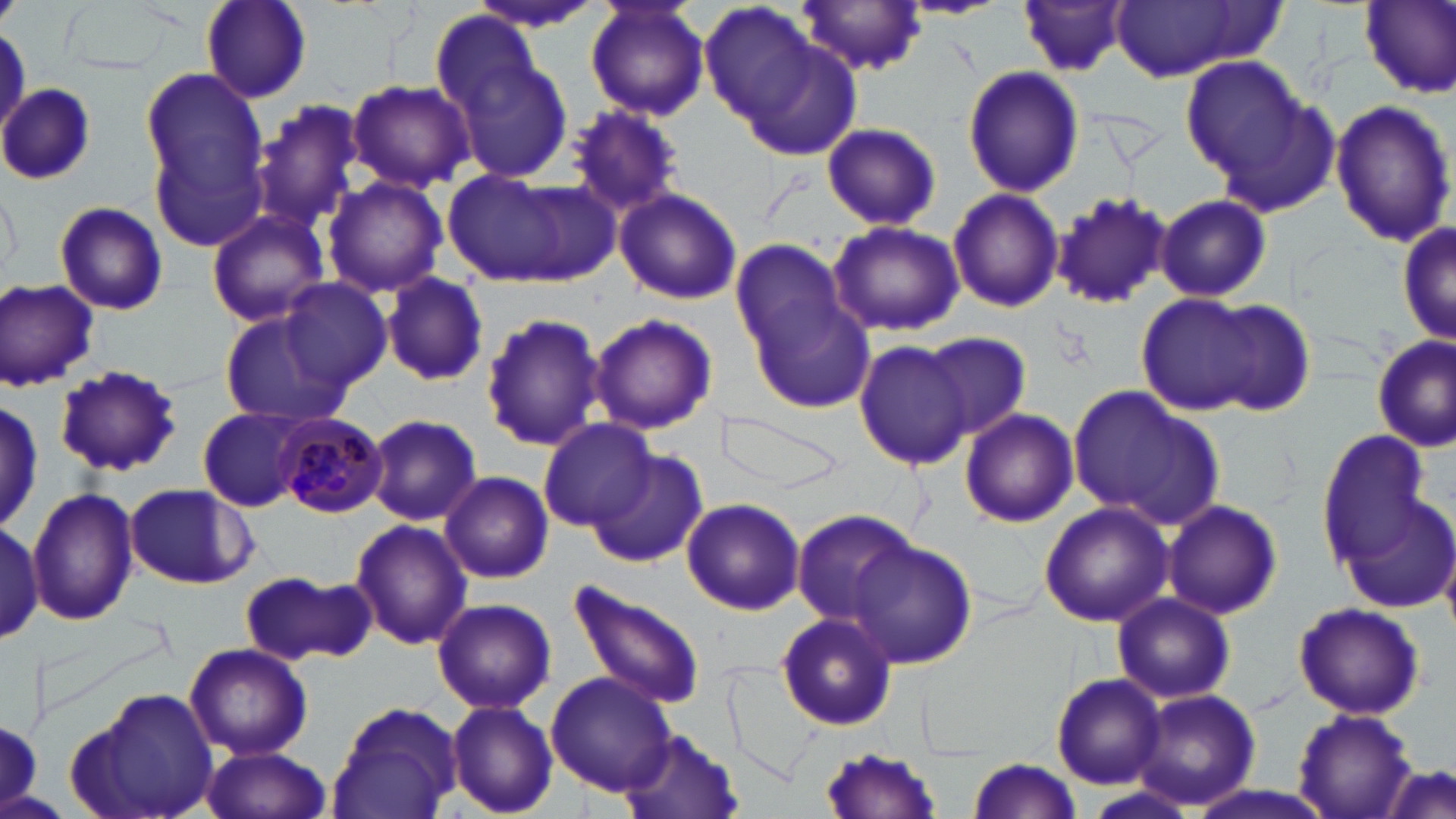
slide-level diagnosis = Plasmodium malariae
field of view = single
uninfected red blood cell locations = approximate bounding boxes as (x1,y1)-(x2,y2) corner pairs in pixels: (196,0)-(311,103), (464,0)-(609,34), (585,0)-(710,123), (901,0)-(1008,20), (1107,0)-(1276,82), (1358,0)-(1456,96), (696,1)-(826,129), (799,1)-(929,76), (1019,1)-(1130,78), (728,24)-(864,161), (437,32)-(573,188), (1180,54)-(1309,188), (961,64)-(1085,198), (139,67)-(267,201), (347,80)-(473,191), (0,82)-(96,184), (1330,97)-(1454,250), (257,101)-(365,228), (564,104)-(686,218), (820,122)-(941,231), (151,135)-(270,257), (443,170)-(597,287), (321,176)-(447,298), (0,185)-(23,284), (947,187)-(1065,314), (615,189)-(742,306), (1051,189)-(1172,310), (1154,194)-(1272,303), (53,201)-(169,316), (203,209)-(332,326), (1395,213)-(1454,352), (829,221)-(964,337), (731,239)-(848,355), (381,271)-(489,387), (277,277)-(392,391), (1,280)-(101,390), (748,289)-(874,412), (1136,292)-(1293,418), (1202,303)-(1318,415), (216,311)-(349,425), (480,311)-(605,451), (586,313)-(720,434), (920,331)-(1030,442), (1371,332)-(1455,452), (853,338)-(975,470), (53,365)-(183,477), (1069,387)-(1225,528), (714,406)-(848,499), (196,407)-(312,512), (960,408)-(1079,528), (365,413)-(482,526), (538,419)-(657,531), (1316,428)-(1435,568), (587,453)-(706,568), (440,471)-(555,585), (123,483)-(256,589), (28,486)-(138,625), (1332,489)-(1456,614), (1162,498)-(1283,620), (684,499)-(805,615), (1037,501)-(1174,629), (789,508)-(921,625), (350,519)-(473,650), (1,520)-(44,645), (846,539)-(975,669), (242,569)-(373,661), (568,580)-(705,709), (1112,593)-(1235,705), (433,597)-(556,714), (1291,601)-(1425,720), (775,611)-(897,729), (184,642)-(313,760), (722,663)-(823,787), (545,669)-(678,797), (1050,672)-(1166,789), (74,686)-(222,819), (1128,687)-(1262,811), (445,699)-(558,817), (326,701)-(463,819), (1292,709)-(1419,819), (2,718)-(44,804), (621,726)-(743,819), (818,743)-(945,819), (200,745)-(332,819), (967,756)-(1084,818), (1379,765)-(1456,819)
image size = 1456×819 pixels
modality = optical microscopy
platelet locations = approximate bounding boxes as (x1,y1)-(x2,y2) corner pairs in pixels: (0,0)-(19,24)
stain = May-Grünwald-Giemsa
preparation = thin blood film
magnification = 1000x
Plasmodium malariae-infected red blood cell locations = approximate bounding boxes as (x1,y1)-(x2,y2) corner pairs in pixels: (277,413)-(388,518)